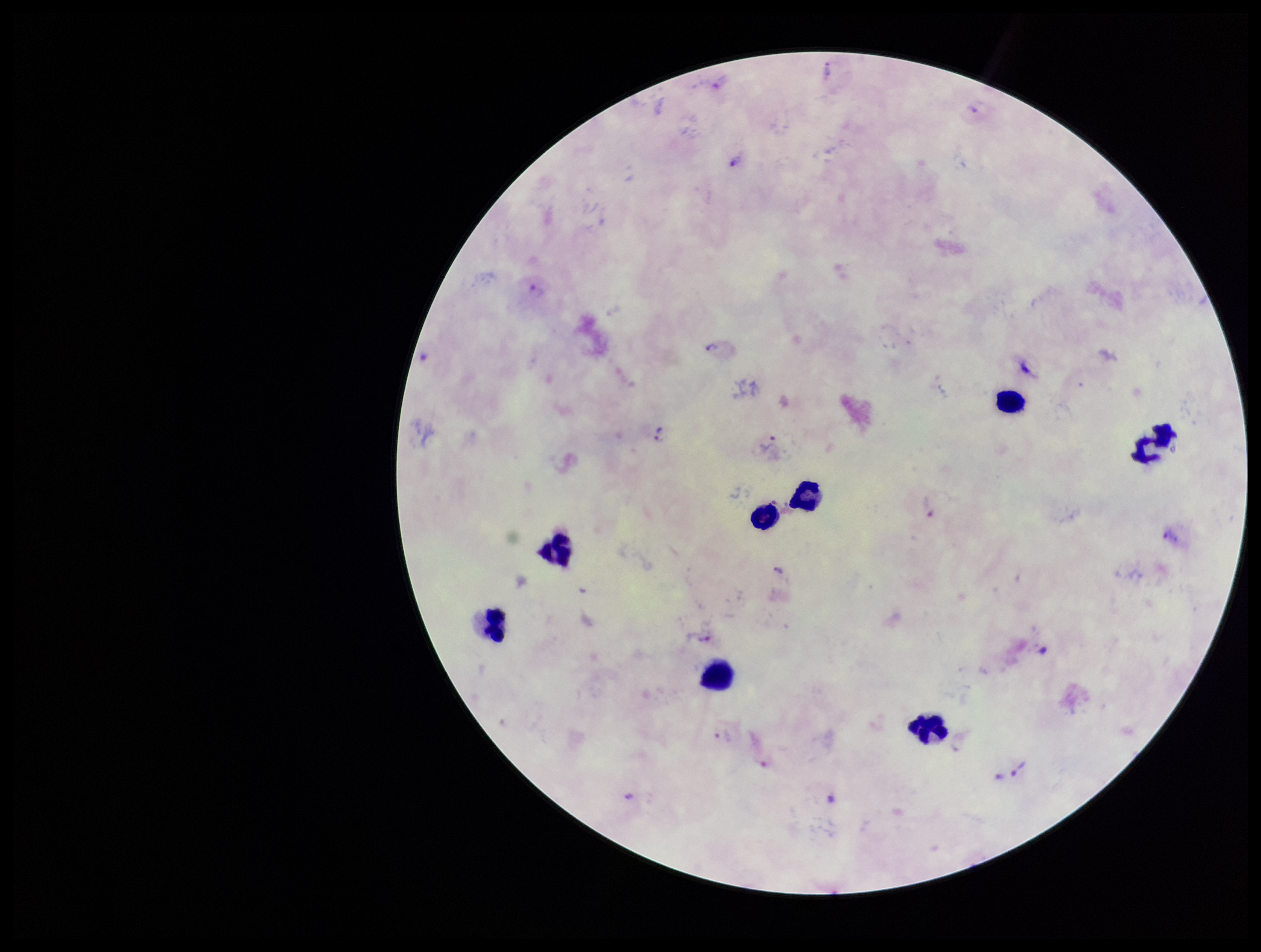

Leukocyte count: 8. Single field of view. Patient malaria status: positive. Stained with Giemsa. Plasmodium parasites: identified. Preparation: thick blood smear. Species reported for this patient: Plasmodium vivax. Parasite count: 13. Image is 1261×952 pixels. Smartphone photograph taken through the eyepiece of a microscope.